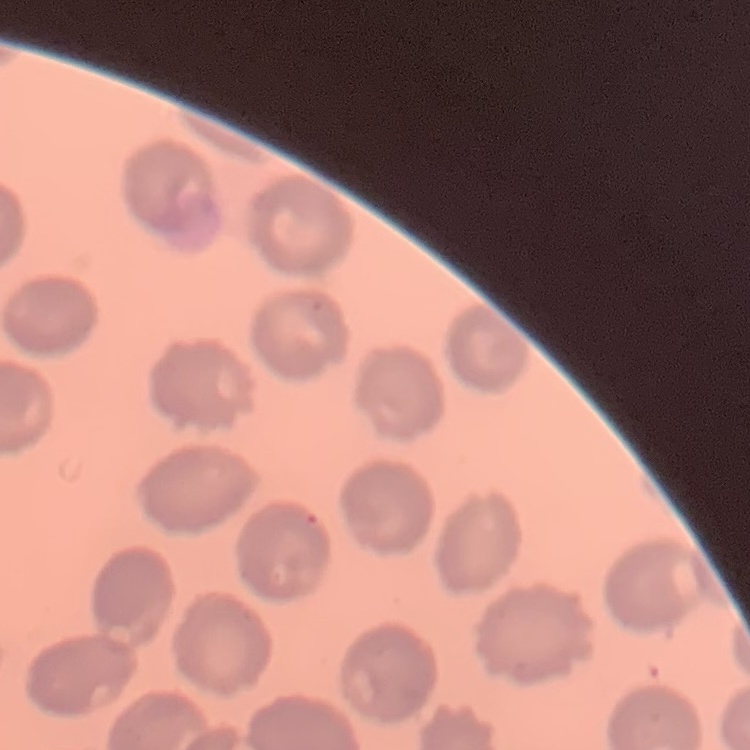
The erythrocytes show no rouleaux formation. Thin peripheral smear. Stained with either Field's or Giemsa. Square crop of a larger photomicrograph.